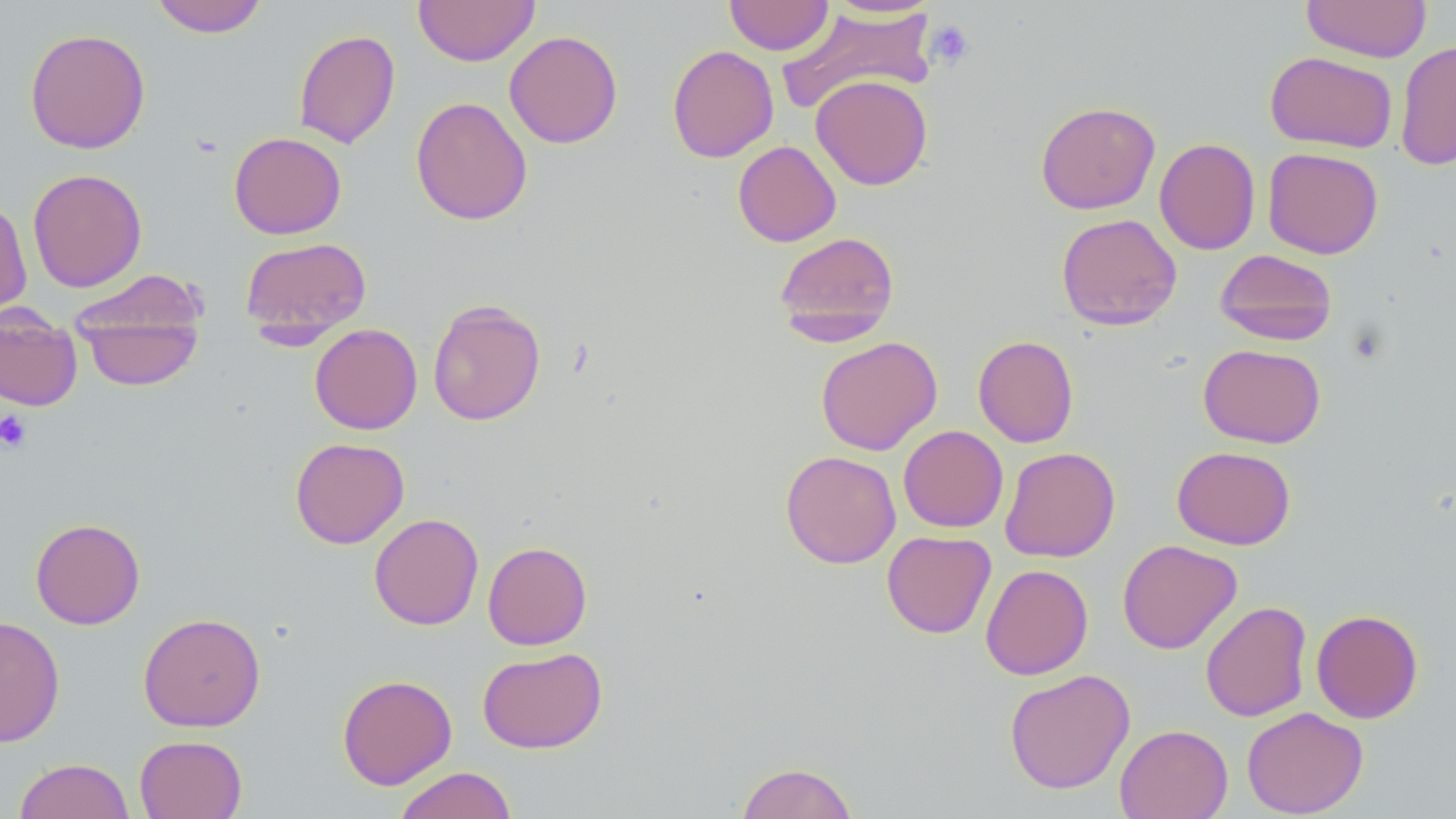

Approximate bounding boxes as (x1,y1)-(x2,y2) corner pairs in pixels. Uninfected red blood cell locations: (151,0)-(269,37), (413,0)-(540,66), (724,0)-(834,55), (820,0)-(942,18), (1301,1)-(1432,62), (777,5)-(938,115), (24,27)-(151,154), (293,29)-(400,149), (503,30)-(623,149), (1395,40)-(1456,171), (667,44)-(779,162), (1265,51)-(1397,153), (810,75)-(933,190), (410,96)-(533,225), (1035,101)-(1160,215), (229,132)-(346,239), (1154,138)-(1260,254), (732,140)-(841,247), (1262,147)-(1383,259), (27,168)-(147,292), (0,198)-(32,318), (1055,213)-(1182,331), (774,231)-(900,343), (239,236)-(372,342), (1215,249)-(1337,346), (69,269)-(208,353), (75,297)-(205,392), (427,299)-(546,426), (0,305)-(83,412), (309,323)-(423,434), (972,335)-(1079,447), (815,336)-(942,455), (1198,343)-(1326,448), (898,425)-(1009,533), (290,437)-(410,549), (1000,446)-(1120,562), (1172,446)-(1296,549), (780,450)-(901,569), (369,513)-(484,630), (30,517)-(146,630), (881,530)-(996,638), (1117,539)-(1242,654), (482,541)-(592,650), (980,564)-(1093,680), (1200,601)-(1312,722), (1311,609)-(1424,724), (138,612)-(266,732), (0,615)-(66,747), (477,646)-(607,753), (1004,668)-(1136,794), (337,674)-(457,789), (1242,707)-(1368,818), (1114,723)-(1233,819), (134,735)-(247,819), (14,758)-(135,819), (735,761)-(858,819), (393,766)-(518,819). Platelet locations: (925,20)-(975,70), (0,411)-(33,453). Slide-level diagnosis: negative for blood parasites. Thin blood smear. 1000x magnification. Image is 1456×819 pixels. Single field of view. Light microscopy. May-Grünwald-Giemsa-stained preparation.